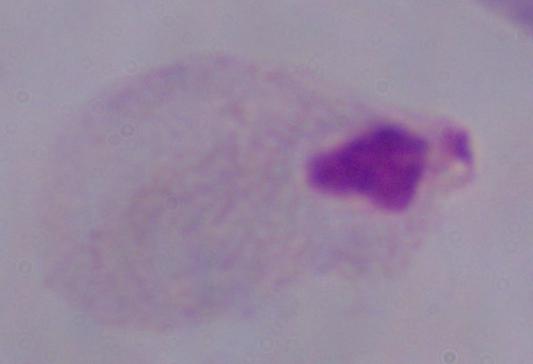
magnification = 1000x
modality = micrograph
identification = trichomonad